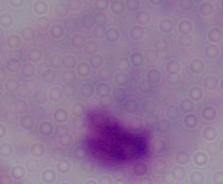

Summary:
  - Identification: trichomonad
  - Magnification: 1000x
  - Modality: photomicrograph